Identify the cell.
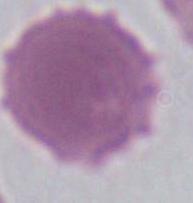
An erythrocyte.

magnification = 1000x
modality = photomicrograph